Assess this cell for malaria.
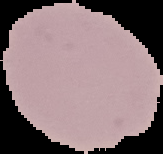

It is uninfected.

image size = 163×154 pixels
preparation = thin blood smear
image type = cell region segmented out of the field of view; surrounding area masked to black